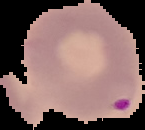

preparation = thin blood film
image type = cell region segmented out of the field of view; surrounding area masked to black
image size = 145×130 pixels
result = malaria parasites detected